Locate platelets.
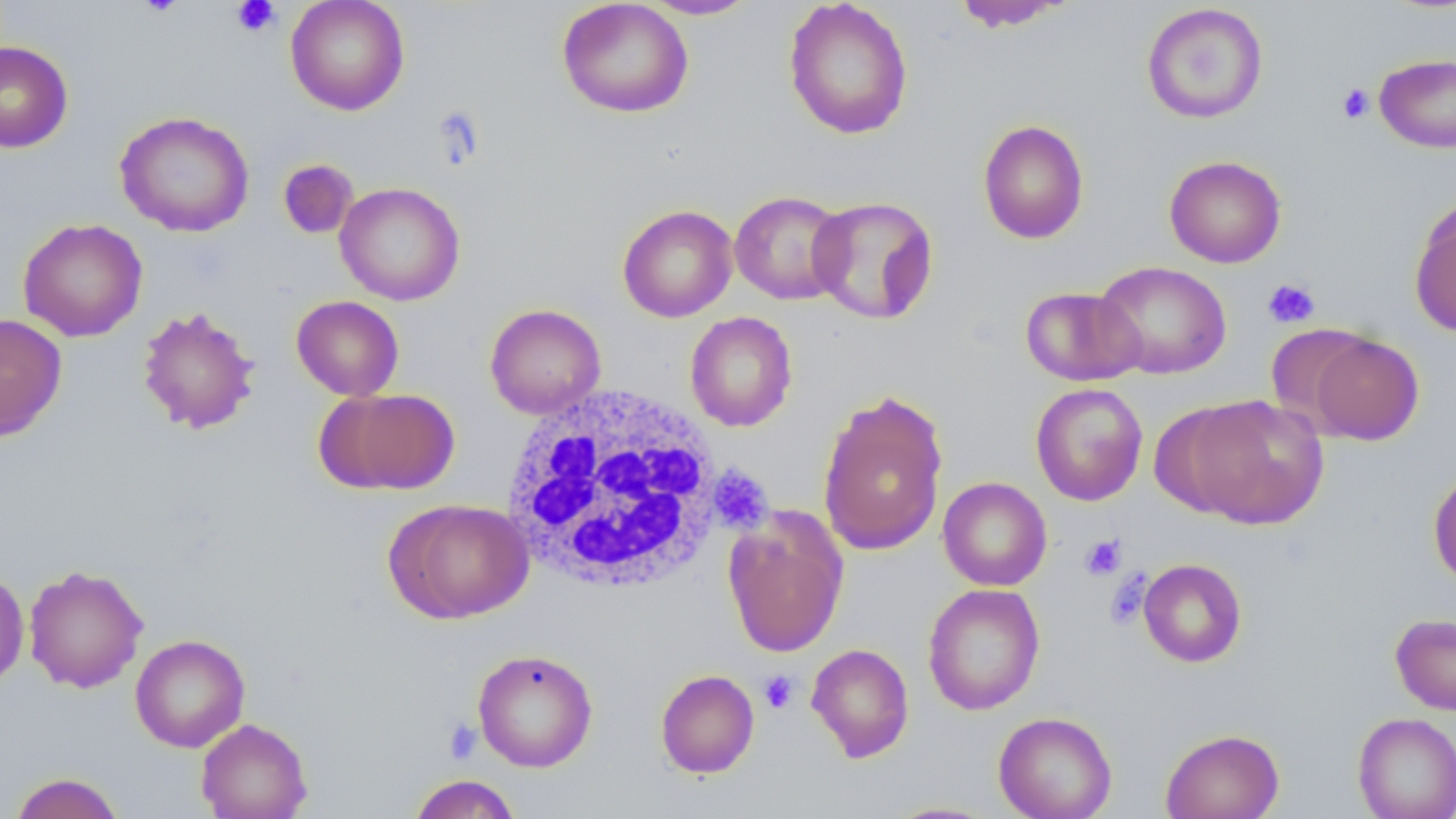
Approximate bounding boxes as (x1, y1, x2, y2) in pixels.
Platelets: (229, 0, 282, 37), (1337, 83, 1375, 124), (1262, 278, 1320, 328), (716, 472, 771, 532), (1080, 534, 1127, 580), (1104, 572, 1151, 630), (759, 670, 798, 714), (443, 718, 482, 764).

slide-level diagnosis = negative for blood parasites
magnification = 1000x
preparation = thin blood film
stain = May-Grünwald-Giemsa
field of view = single
white blood cell locations = approximate bounding boxes as (x1, y1, x2, y2) in pixels: (500, 384, 725, 595)
image size = 1456×819 pixels
modality = optical microscopy
uninfected red blood cell locations = approximate bounding boxes as (x1, y1, x2, y2) in pixels: (285, 0, 410, 116), (557, 0, 694, 119), (639, 0, 760, 21), (783, 0, 914, 140), (951, 1, 1073, 32), (1141, 3, 1269, 124), (0, 41, 73, 153), (1374, 53, 1456, 152), (115, 111, 254, 238), (977, 118, 1089, 244), (1163, 155, 1287, 268), (277, 159, 358, 238), (335, 182, 465, 306), (729, 191, 851, 305), (807, 195, 940, 325), (1410, 199, 1456, 338), (617, 204, 738, 322), (17, 218, 148, 342), (1093, 260, 1232, 380), (1020, 285, 1144, 386), (291, 295, 404, 400), (485, 303, 606, 418), (137, 305, 260, 435), (684, 311, 798, 432), (0, 313, 67, 442), (1264, 325, 1376, 432), (1305, 332, 1424, 445), (1030, 382, 1148, 506), (317, 387, 460, 496), (818, 389, 949, 556), (1179, 395, 1329, 529), (1428, 466, 1456, 589), (938, 477, 1052, 591), (385, 498, 534, 624), (723, 511, 849, 658), (1137, 558, 1247, 667), (23, 565, 148, 693), (0, 569, 29, 689), (922, 583, 1045, 715), (1389, 613, 1456, 717), (130, 633, 250, 752), (806, 643, 914, 762), (472, 648, 598, 772), (655, 669, 760, 778), (993, 711, 1117, 819), (1352, 712, 1456, 819), (195, 718, 312, 818), (1160, 727, 1285, 819), (8, 772, 125, 819), (406, 773, 524, 819), (882, 801, 1001, 818)